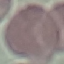
malaria status = uninfected
capture = smartphone camera at the microscope eyepiece
preparation = thin blood film
image type = cell patch, automatically extracted from a larger field of view and resized to 64 × 64 pixels
stain = Giemsa